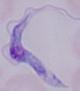

Summary:
  - Identification: trypanosome
  - Modality: photomicrograph
  - Magnification: 1000x